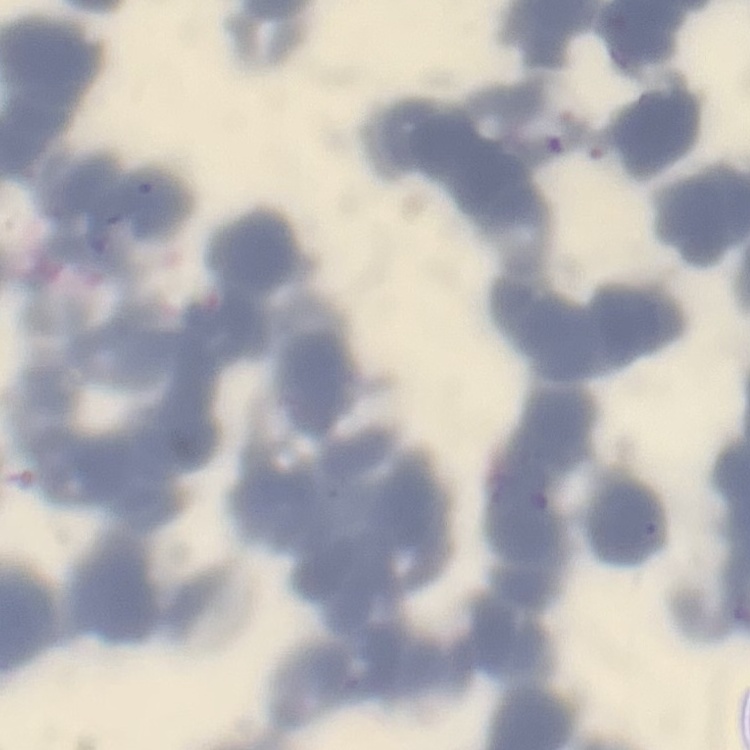

{
  "erythrocyte_morphology": "rouleaux formation",
  "preparation": "thin blood smear",
  "image_type": "one tile cut from a larger photomicrograph",
  "stain": "Field's or Giemsa"
}